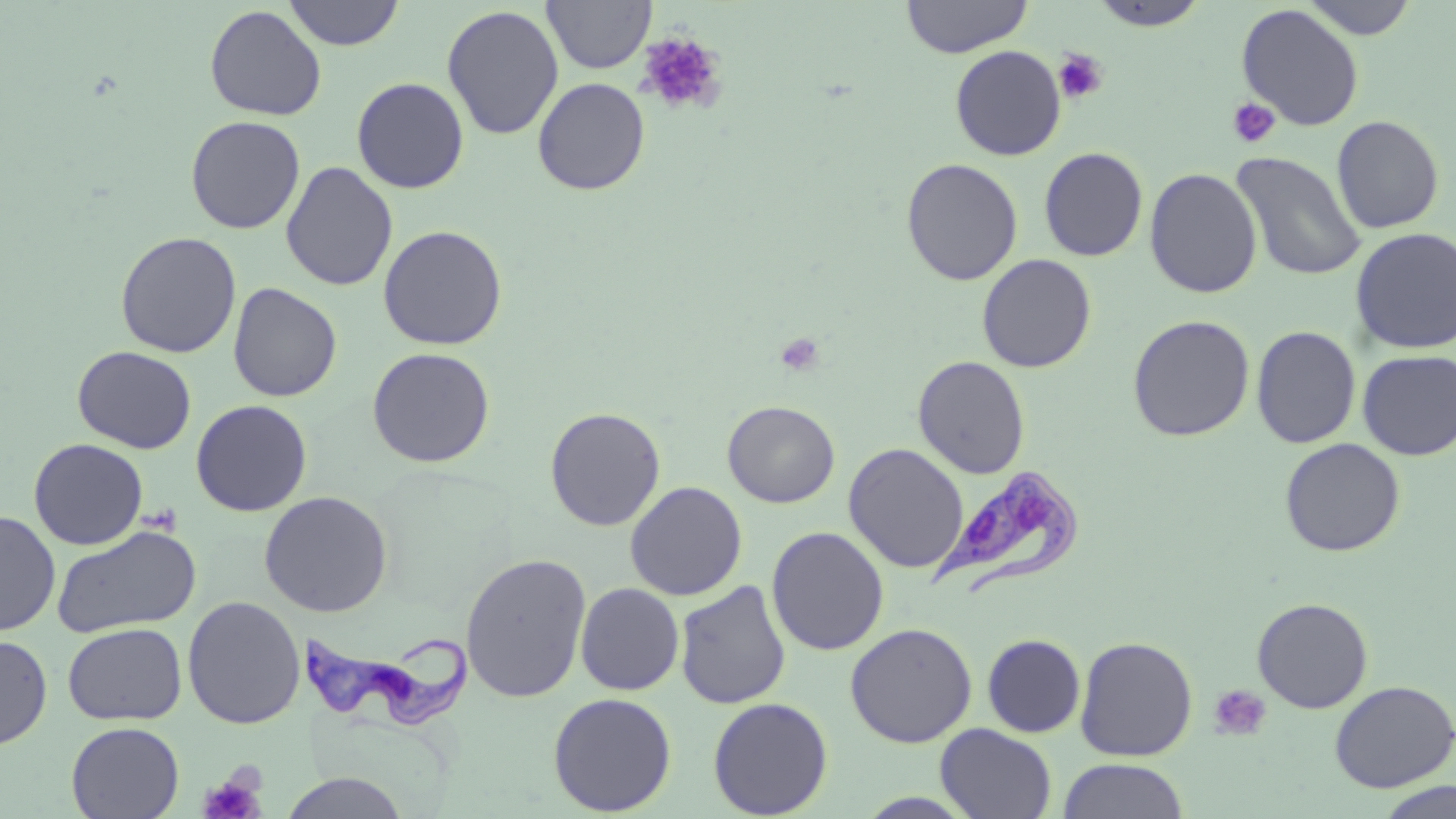

Approximate bounding boxes as [x1, y1, x2, y2] in pixels. Uninfected red blood cell locations: [283, 0, 404, 50], [901, 0, 1031, 58], [1300, 0, 1420, 39], [542, 1, 656, 74], [1089, 1, 1210, 31], [204, 4, 326, 121], [1236, 4, 1365, 130], [442, 5, 564, 141], [950, 44, 1066, 161], [351, 77, 470, 194], [532, 77, 650, 195], [185, 115, 305, 234], [1331, 115, 1444, 233], [1038, 147, 1148, 262], [1231, 151, 1366, 281], [901, 158, 1023, 286], [281, 161, 398, 291], [1144, 168, 1263, 298], [378, 224, 508, 350], [1350, 227, 1456, 355], [115, 231, 242, 358], [976, 253, 1097, 373], [228, 282, 342, 402], [1127, 315, 1255, 441], [1251, 325, 1362, 449], [72, 345, 197, 454], [366, 347, 496, 468], [1357, 349, 1456, 460], [912, 355, 1030, 478], [191, 399, 312, 517], [722, 400, 840, 508], [544, 406, 666, 531], [29, 438, 148, 550], [1279, 438, 1406, 557], [843, 443, 969, 573], [625, 481, 748, 601], [259, 491, 393, 616], [0, 511, 60, 636], [51, 524, 202, 639], [767, 526, 889, 656], [460, 552, 592, 703], [674, 580, 792, 709], [575, 582, 685, 695], [182, 596, 305, 729], [1252, 597, 1374, 713], [63, 622, 186, 725], [845, 622, 978, 748], [0, 633, 52, 750], [981, 634, 1086, 737], [1074, 636, 1198, 761], [1329, 680, 1456, 793], [548, 692, 677, 816], [707, 697, 833, 818], [66, 722, 184, 819], [935, 724, 1057, 819], [1056, 758, 1190, 819], [279, 772, 410, 818], [1377, 781, 1456, 819]. Platelet locations: [636, 31, 727, 116], [1053, 48, 1108, 104], [1227, 97, 1281, 149], [775, 332, 824, 376], [1207, 683, 1273, 742], [198, 773, 266, 819]. Trypanosoma brucei locations: [930, 465, 1084, 598], [299, 621, 477, 728]. Slide-level diagnosis: Trypanosoma brucei. May-Grünwald-Giemsa stain. Thin blood smear. Single field of view. Light microscopy. Image is 1456×819 pixels. 1000x magnification.